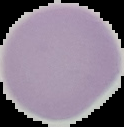
Summary:
  - Image size: 124×127 pixels
  - Preparation: thin blood film
  - Result: negative for Plasmodium parasites
  - Image type: cell region segmented out of the field of view; surrounding area masked to black